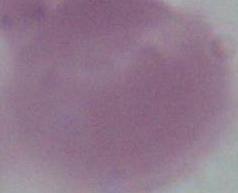
Summary:
  - Magnification: 1000x
  - Modality: micrograph
  - Identification: erythrocyte